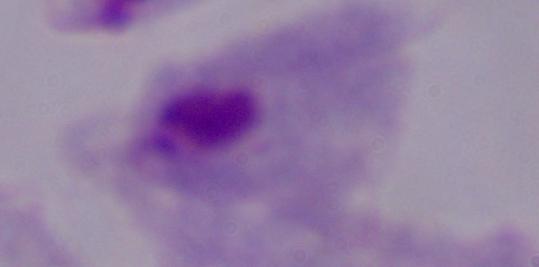

identification = trichomonad
magnification = 1000x
modality = photomicrograph